Locate every Plasmodium malariae-infected red blood cell.
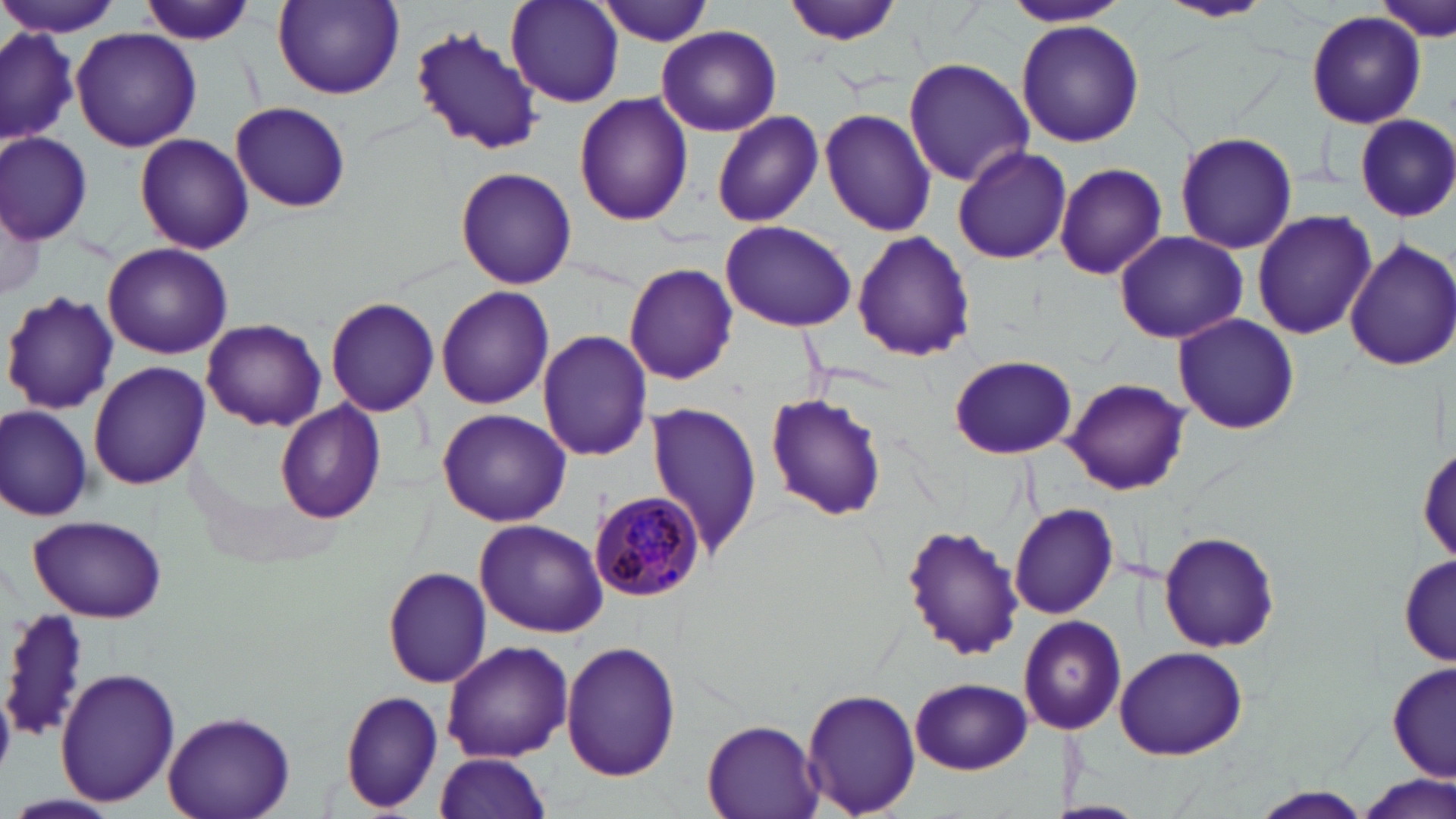

Approximate bounding boxes as named x1/y1/x2/y2 corners in pixels.
Plasmodium malariae-infected red blood cells: (x1=589, y1=490, x2=705, y2=602).

Summary:
  - Uninfected red blood cell locations: (x1=0, y1=0, x2=126, y2=39), (x1=136, y1=0, x2=254, y2=47), (x1=505, y1=0, x2=624, y2=107), (x1=782, y1=0, x2=908, y2=47), (x1=1002, y1=0, x2=1132, y2=28), (x1=1158, y1=0, x2=1272, y2=23), (x1=1374, y1=0, x2=1455, y2=43), (x1=272, y1=1, x2=404, y2=99), (x1=594, y1=1, x2=717, y2=45), (x1=1306, y1=11, x2=1427, y2=130), (x1=1017, y1=20, x2=1144, y2=148), (x1=0, y1=24, x2=79, y2=148), (x1=409, y1=26, x2=543, y2=158), (x1=656, y1=26, x2=780, y2=137), (x1=71, y1=28, x2=200, y2=153), (x1=904, y1=57, x2=1034, y2=185), (x1=928, y1=80, x2=1061, y2=249), (x1=575, y1=94, x2=694, y2=227), (x1=230, y1=101, x2=352, y2=210), (x1=819, y1=108, x2=938, y2=237), (x1=711, y1=110, x2=824, y2=227), (x1=1354, y1=113, x2=1456, y2=222), (x1=1174, y1=131, x2=1299, y2=254), (x1=1, y1=133, x2=91, y2=243), (x1=136, y1=135, x2=253, y2=254), (x1=951, y1=144, x2=1072, y2=266), (x1=1053, y1=162, x2=1169, y2=281), (x1=456, y1=166, x2=577, y2=290), (x1=2, y1=193, x2=45, y2=307), (x1=1252, y1=209, x2=1377, y2=339), (x1=721, y1=219, x2=858, y2=332), (x1=1114, y1=231, x2=1247, y2=344), (x1=851, y1=232, x2=976, y2=362), (x1=1346, y1=238, x2=1456, y2=372), (x1=103, y1=243, x2=232, y2=361), (x1=624, y1=263, x2=738, y2=386), (x1=436, y1=286, x2=555, y2=409), (x1=2, y1=291, x2=117, y2=413), (x1=325, y1=297, x2=439, y2=417), (x1=1173, y1=315, x2=1303, y2=434), (x1=202, y1=319, x2=326, y2=431), (x1=537, y1=331, x2=653, y2=462), (x1=950, y1=355, x2=1077, y2=459), (x1=89, y1=359, x2=210, y2=489), (x1=1064, y1=378, x2=1189, y2=495), (x1=764, y1=394, x2=884, y2=520), (x1=276, y1=399, x2=388, y2=523), (x1=644, y1=400, x2=764, y2=560), (x1=0, y1=405, x2=92, y2=521), (x1=436, y1=408, x2=572, y2=527), (x1=1418, y1=442, x2=1454, y2=566), (x1=1008, y1=502, x2=1119, y2=619), (x1=26, y1=514, x2=167, y2=621), (x1=474, y1=520, x2=606, y2=637), (x1=901, y1=525, x2=1024, y2=658), (x1=1159, y1=532, x2=1281, y2=652), (x1=1399, y1=550, x2=1452, y2=669), (x1=383, y1=567, x2=492, y2=689), (x1=5, y1=607, x2=95, y2=742), (x1=1019, y1=615, x2=1126, y2=733), (x1=441, y1=639, x2=573, y2=763), (x1=561, y1=639, x2=683, y2=781), (x1=1114, y1=645, x2=1248, y2=759), (x1=1388, y1=661, x2=1454, y2=786), (x1=55, y1=667, x2=181, y2=808), (x1=911, y1=677, x2=1031, y2=774), (x1=802, y1=686, x2=920, y2=816), (x1=338, y1=689, x2=443, y2=812), (x1=162, y1=708, x2=294, y2=818), (x1=701, y1=721, x2=822, y2=818), (x1=431, y1=753, x2=556, y2=818), (x1=1352, y1=776, x2=1455, y2=819), (x1=1245, y1=787, x2=1375, y2=819), (x1=9, y1=793, x2=120, y2=817)
  - Slide-level diagnosis: Plasmodium malariae
  - Modality: light microscopy
  - Field of view: single
  - Preparation: thin blood film
  - Stain: May-Grünwald-Giemsa
  - Magnification: 1000x
  - Image size: 1456×819 pixels